Classify this cell by malaria status.
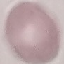
It is uninfected.

preparation = thin smear
stain = Giemsa
capture = smartphone camera at the microscope eyepiece
image type = cell patch, automatically extracted from a larger field of view and resized to 64 × 64 pixels